State which parasite is depicted.
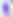

Toxoplasma gondii.

Summary:
  - Magnification: 400x
  - Modality: micrograph